Classify this cell by malaria status.
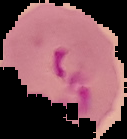

It is parasitized.

{
  "preparation": "thin blood smear",
  "image_size": "127×139 pixels",
  "image_type": "segmented cell region with the area outside set to black"
}